Assess this cell for malaria.
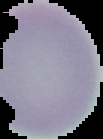

It is uninfected.

image type = segmented cell region with the area outside set to black
image size = 103×139 pixels
preparation = thin blood film